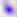 Photomicrograph. Captured at 400x magnification. Toxoplasma gondii is shown.